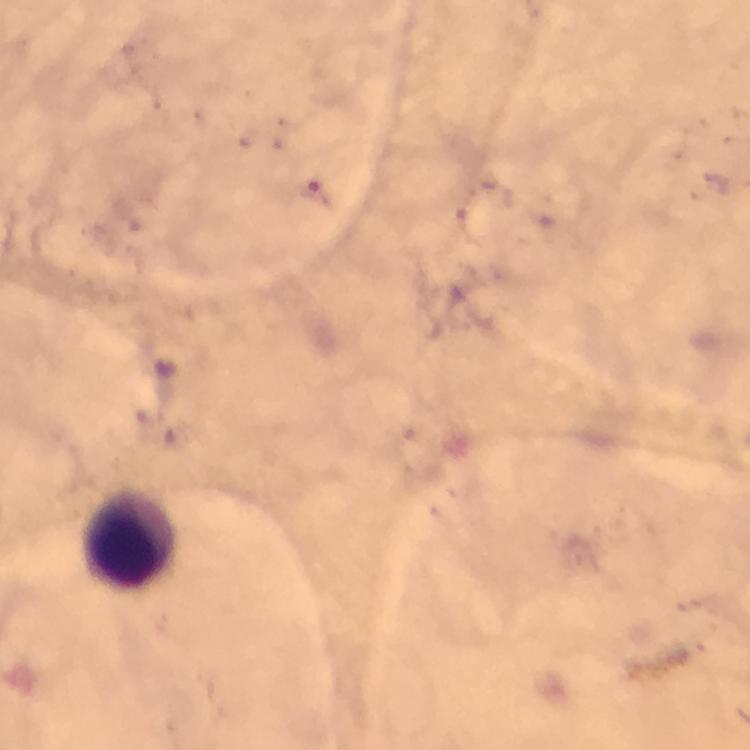

Approximate centers as [x, y] in pixels.
Summary:
  - Leukocyte locations: [128, 539]
  - Malaria parasites: none seen
  - Immersion oil: used
  - Capture: smartphone camera through the microscope
  - Image size: 750×750 pixels
  - Magnification: 100x
  - Stain: Giemsa
  - Preparation: thick blood film
  - Context: from a diagnostic examination for malaria
  - Cropped from: a single field of view